Assess the morphology of the red blood cells.
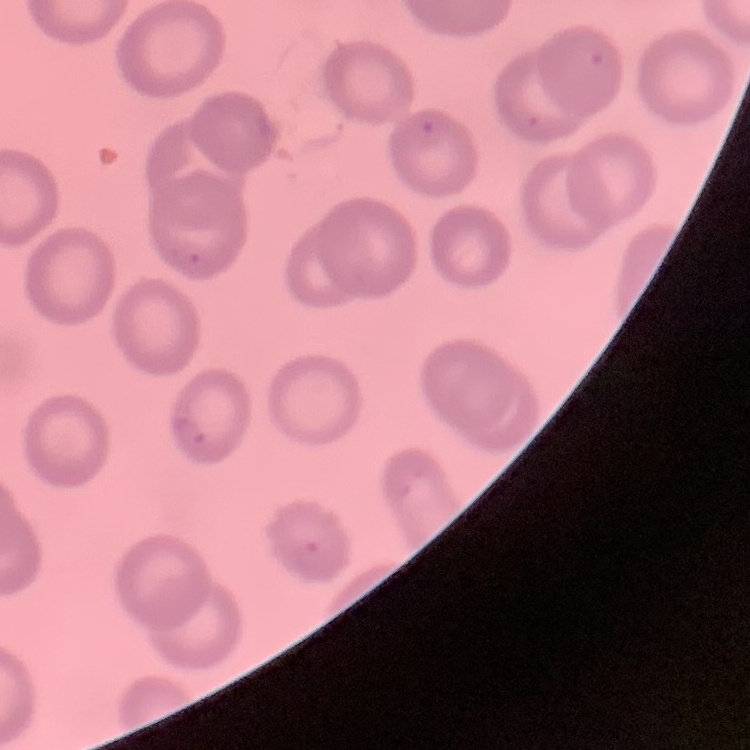
No rouleaux formation.

Field's or Giemsa stain. One tile cut from a larger photomicrograph. Thin peripheral smear.